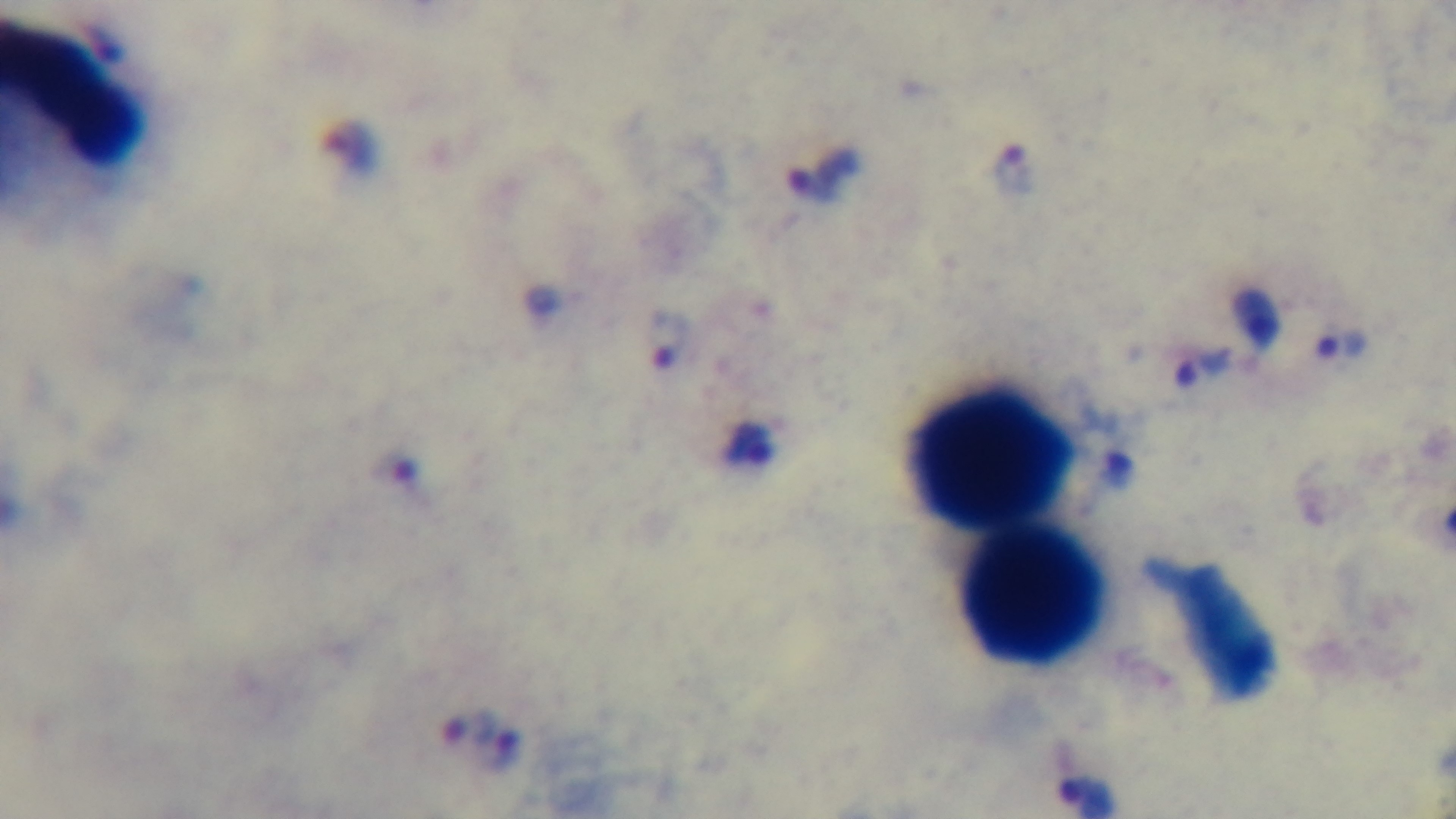

Giemsa-stained. Mounted 4K digital camera. Photomicrograph. Malaria status: positive. Preparation: thick blood film. Oil-immersion objective, 100x. Single field of view.